Report the malaria status of this cell.
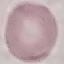
It is uninfected.

Summary:
  - Preparation: thin blood film
  - Capture: smartphone through the microscope eyepiece
  - Stain: Giemsa
  - Image type: automatically extracted cell patch, resized to 64 × 64 pixels